Identify the parasite.
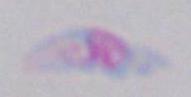

This is Toxoplasma gondii.

modality: photomicrograph
magnification: 1000x